Assess this cell for malaria.
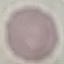
It is uninfected.

stain = Giemsa
image type = automatically extracted cell patch, resized to 64 × 64 pixels
capture = smartphone camera at the microscope eyepiece
preparation = thin blood film